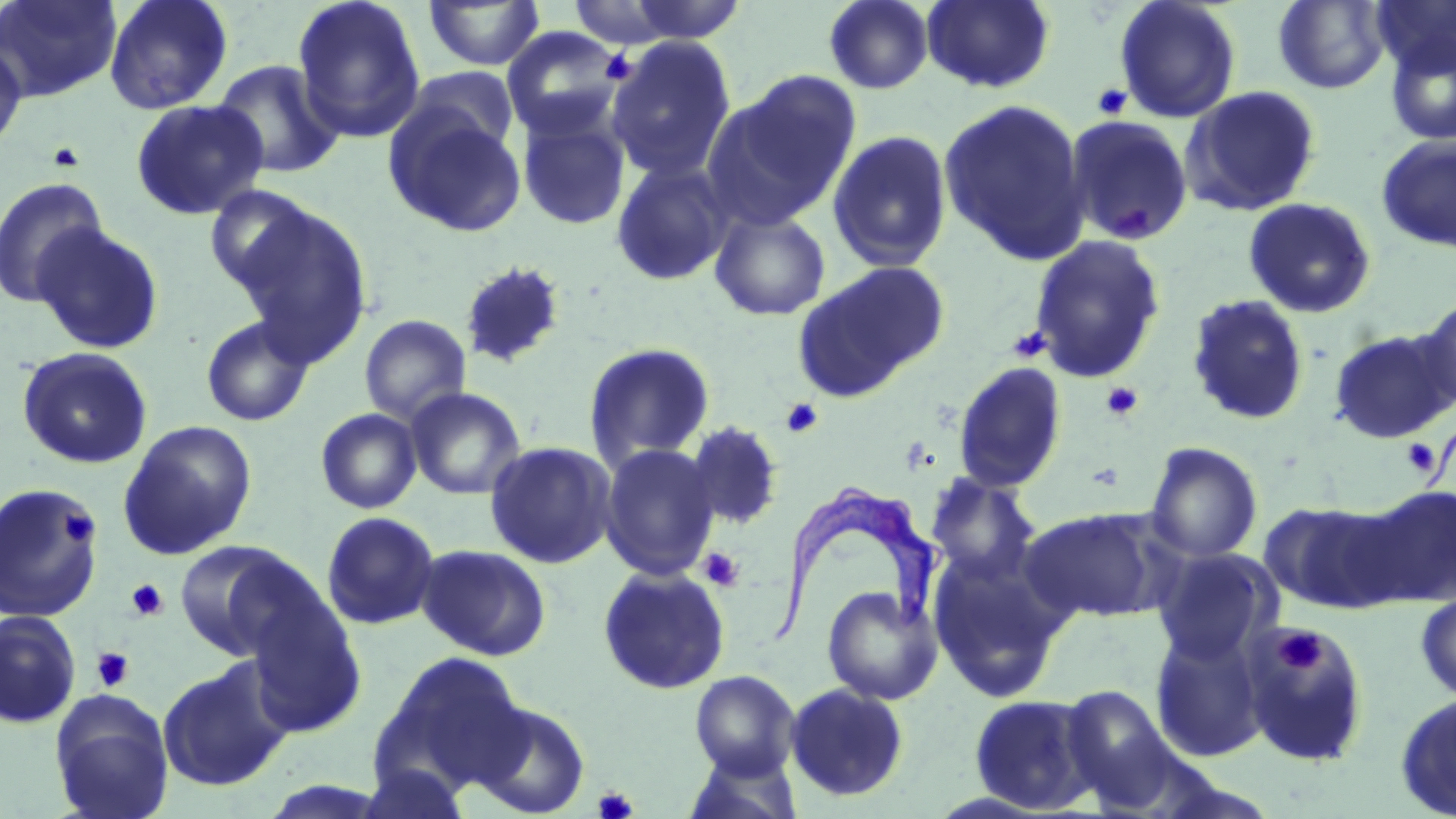
Approximate bounding boxes as (x1, y1, x2, y2) in pixels. Platelet locations: (600, 49, 635, 84), (1091, 83, 1132, 119), (46, 141, 86, 172), (1110, 202, 1157, 241), (1008, 325, 1051, 364), (1101, 381, 1143, 422), (781, 398, 823, 438), (1400, 437, 1441, 478), (56, 510, 98, 548), (698, 547, 744, 591), (126, 579, 168, 622), (1274, 627, 1328, 676), (91, 647, 134, 691), (593, 786, 638, 819). Trypanosoma brucei locations: (765, 485, 939, 649). Uninfected red blood cell locations: (0, 0, 121, 102), (103, 0, 234, 115), (291, 0, 426, 144), (622, 0, 749, 44), (823, 0, 934, 94), (922, 0, 1055, 93), (1273, 0, 1391, 94), (1371, 0, 1456, 77), (422, 1, 546, 71), (564, 1, 690, 49), (1114, 1, 1241, 123), (501, 28, 626, 140), (1385, 34, 1456, 145), (605, 36, 737, 183), (0, 41, 29, 154), (211, 59, 344, 179), (401, 67, 519, 163), (717, 71, 862, 222), (1181, 85, 1322, 216), (937, 98, 1092, 265), (130, 99, 269, 220), (383, 102, 528, 238), (516, 110, 631, 231), (1065, 114, 1194, 246), (826, 129, 953, 272), (1375, 134, 1456, 253), (610, 160, 733, 287), (0, 177, 109, 308), (203, 185, 319, 298), (1243, 197, 1377, 318), (231, 206, 373, 364), (709, 208, 831, 321), (32, 223, 164, 354), (1028, 234, 1165, 383), (793, 260, 949, 400), (457, 261, 568, 370), (1186, 294, 1310, 426), (1415, 298, 1456, 415), (359, 314, 471, 425), (200, 316, 315, 427), (1328, 328, 1456, 443), (583, 342, 716, 470), (17, 347, 153, 470), (952, 361, 1068, 493), (405, 387, 526, 500), (315, 408, 422, 514), (118, 420, 257, 560), (683, 420, 785, 531), (484, 441, 618, 569), (1145, 442, 1263, 563), (598, 443, 721, 581), (925, 474, 1041, 587), (0, 482, 103, 625), (1354, 483, 1456, 608), (1258, 499, 1400, 613), (1021, 507, 1166, 623), (321, 511, 440, 630), (173, 539, 310, 660), (416, 544, 552, 661), (927, 547, 1067, 703), (1151, 547, 1281, 664), (597, 565, 731, 694), (822, 585, 942, 705), (1415, 591, 1456, 703), (240, 594, 367, 738), (0, 610, 81, 729), (1240, 624, 1370, 766), (1150, 629, 1268, 762), (376, 651, 527, 790), (156, 658, 292, 792), (689, 670, 800, 778), (784, 683, 910, 802), (1058, 685, 1176, 807), (49, 689, 174, 819), (1394, 691, 1456, 818), (968, 694, 1100, 813), (472, 699, 590, 817), (681, 749, 803, 819), (357, 761, 472, 819). Slide-level diagnosis: Trypanosoma brucei. May-Grünwald-Giemsa stain. One field of a larger specimen. Image is 1456×819 pixels. Light microscopy. Thin blood smear. Captured at 1000x magnification.